Evaluate for Plasmodium parasites.
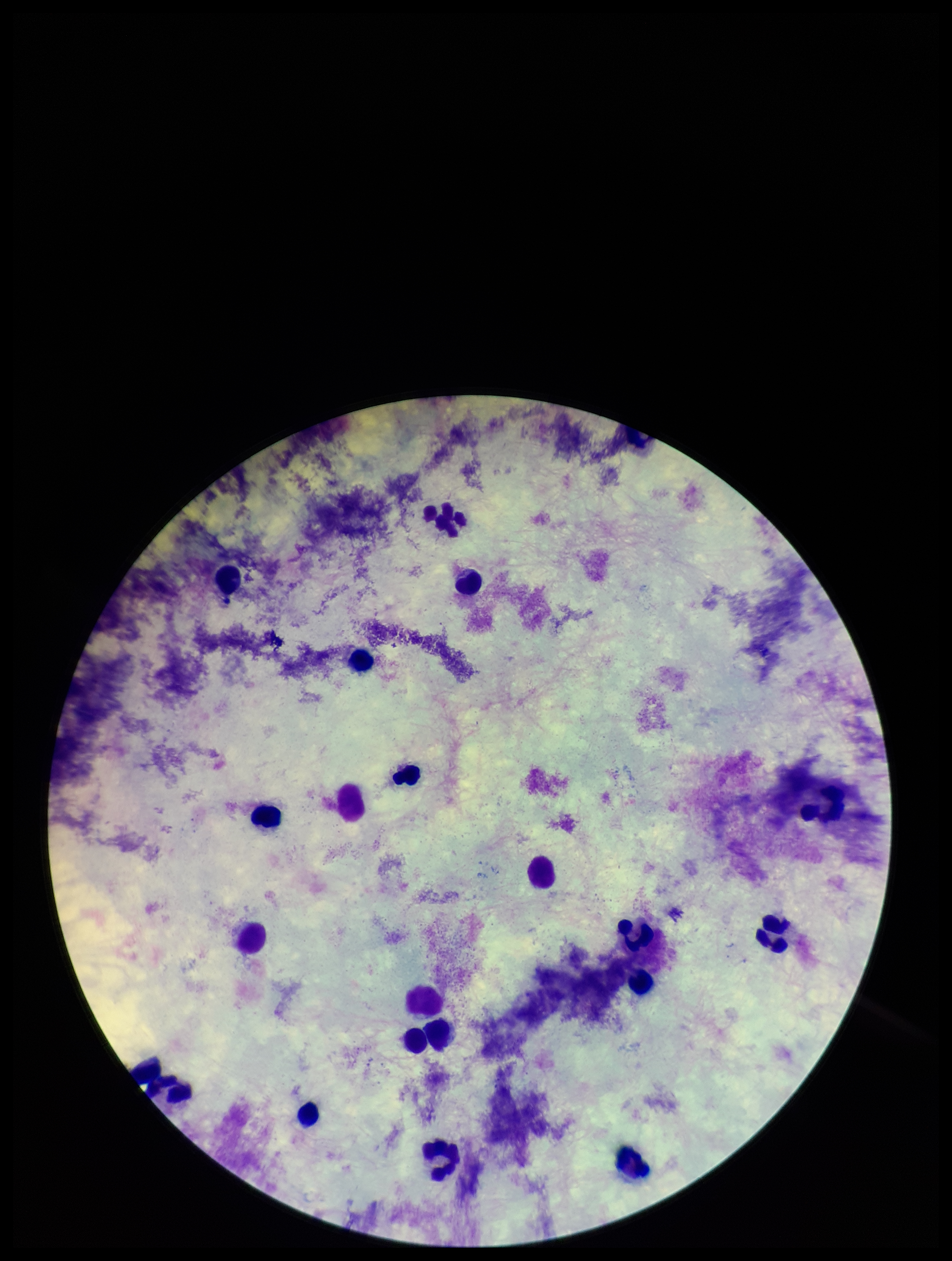

None seen.

patient malaria status = negative
parasite count = 0
field of view = single
image size = 952×1261 pixels
capture = smartphone photograph through the microscope eyepiece
stain = Giemsa
leukocyte count = 20
preparation = thick blood smear